Classify this cell by malaria status.
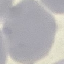
Uninfected.

Summary:
  - Image type: automatically extracted cell patch, resized to 64 × 64 pixels
  - Capture: smartphone camera at the microscope eyepiece
  - Stain: Giemsa
  - Preparation: thin blood smear